Report the malaria status of this cell.
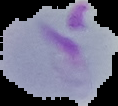
It is parasitized.

Image is 118×106 pixels. From a thin blood film. Segmented cell region on a black background.